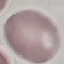

Summary:
  - Result: no malaria parasites seen
  - Preparation: thin smear
  - Image type: automatically extracted cell patch, resized to 64 × 64 pixels
  - Stain: Giemsa
  - Capture: smartphone camera at the microscope eyepiece